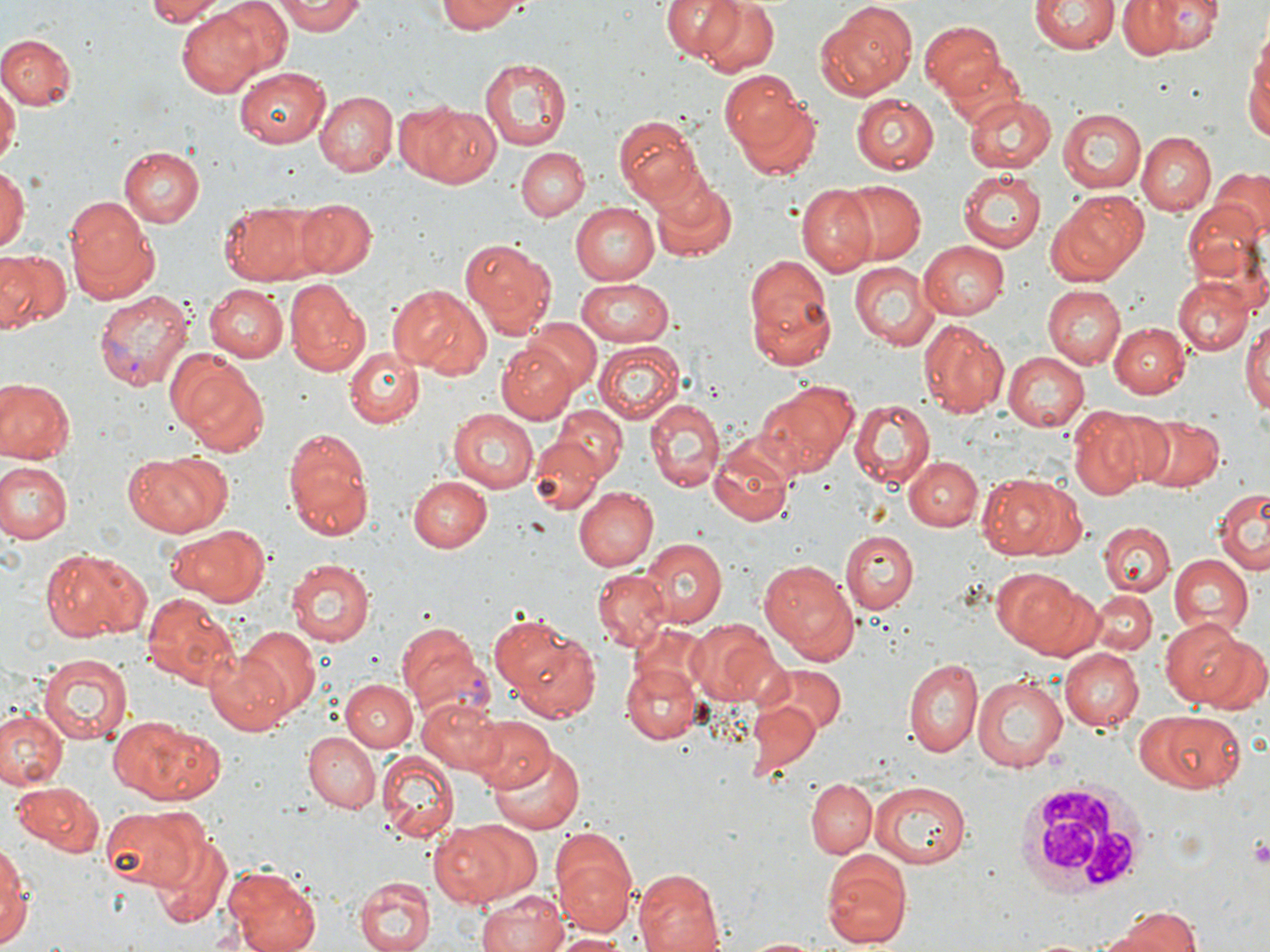
Approximate bounding boxes as (x1,y1)-(x2,y2) corner pairs in pixels. Uninfected red blood cell locations: (145,0)-(225,25), (206,0)-(291,81), (274,0)-(365,35), (433,0)-(527,33), (656,0)-(747,66), (692,0)-(780,77), (1117,0)-(1222,59), (1029,1)-(1118,56), (814,2)-(918,102), (178,10)-(266,98), (918,20)-(1006,101), (1,33)-(77,109), (1245,50)-(1270,146), (479,56)-(572,152), (233,68)-(330,147), (0,78)-(18,174), (726,83)-(822,178), (314,90)-(397,176), (964,92)-(1055,174), (851,94)-(939,171), (304,99)-(480,178), (398,102)-(502,190), (1058,107)-(1147,192), (611,114)-(705,206), (1137,132)-(1215,213), (515,147)-(587,220), (120,148)-(203,226), (0,164)-(27,252), (1208,166)-(1268,237), (957,171)-(1047,253), (647,173)-(738,265), (838,180)-(926,263), (796,183)-(877,276), (1050,189)-(1151,283), (64,195)-(158,300), (1185,196)-(1269,297), (294,199)-(376,278), (220,202)-(316,282), (570,203)-(657,285), (458,237)-(557,338), (916,240)-(1011,319), (0,250)-(69,335), (742,253)-(834,365), (850,262)-(939,351), (575,274)-(674,343), (1172,275)-(1252,356), (284,279)-(367,374), (388,284)-(490,378), (1042,284)-(1126,369), (203,285)-(288,362), (1242,316)-(1269,413), (523,319)-(602,395), (918,320)-(1005,417), (1108,321)-(1191,397), (595,343)-(686,426), (496,344)-(576,423), (165,348)-(267,452), (343,349)-(424,427), (1003,351)-(1090,430), (0,379)-(74,463), (753,383)-(853,480), (644,398)-(723,491), (849,399)-(935,490), (452,406)-(539,491), (1068,406)-(1158,496), (553,407)-(626,483), (1141,416)-(1224,493), (282,428)-(372,537), (529,430)-(610,516), (709,434)-(797,527), (122,450)-(233,537), (904,456)-(982,531), (0,461)-(71,544), (979,472)-(1082,563), (409,475)-(494,551), (574,487)-(658,571), (1216,487)-(1269,574), (1099,522)-(1174,596), (166,525)-(268,604), (840,528)-(918,611), (641,539)-(726,624), (40,548)-(147,642), (1168,553)-(1253,638), (286,559)-(374,647), (758,559)-(858,665), (592,568)-(670,652), (1005,572)-(1101,659), (1089,590)-(1157,656), (142,596)-(242,689), (488,612)-(578,692), (686,619)-(780,702), (1164,619)-(1253,705), (505,621)-(605,718), (234,626)-(321,718), (1060,646)-(1143,728), (206,650)-(298,736), (38,653)-(135,746), (903,656)-(984,759), (620,660)-(701,745), (756,662)-(845,735), (971,672)-(1068,773), (342,679)-(417,752), (417,696)-(507,777), (747,699)-(822,779), (1135,707)-(1249,794), (0,709)-(67,789), (105,715)-(225,803), (471,716)-(555,794), (301,731)-(379,813), (485,738)-(589,836), (376,752)-(458,842), (807,778)-(877,858), (868,781)-(972,868), (12,782)-(104,854), (98,803)-(201,890), (432,820)-(532,907), (148,831)-(231,929), (551,833)-(638,936), (0,839)-(30,949), (819,848)-(912,951), (222,867)-(321,952), (630,869)-(727,952), (353,875)-(432,952), (474,890)-(572,952), (1098,908)-(1202,952), (552,930)-(627,951). White blood cell locations: (1012,777)-(1158,899). Platelet locations: (1175,6)-(1204,32), (1248,834)-(1270,865). Plasmodium vivax-infected red blood cell locations: (93,288)-(193,394), (395,621)-(490,717). Slide-level diagnosis: Plasmodium vivax. Thin blood film. One field of a larger specimen. May-Grünwald-Giemsa stain. Optical microscopy. Image is 1270×952 pixels. Captured at 1000x magnification.